Report the malaria status of this cell.
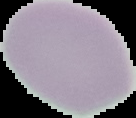

It is uninfected.

preparation = thin blood film
image type = cell region segmented out of the field of view; surrounding area masked to black
image size = 136×118 pixels